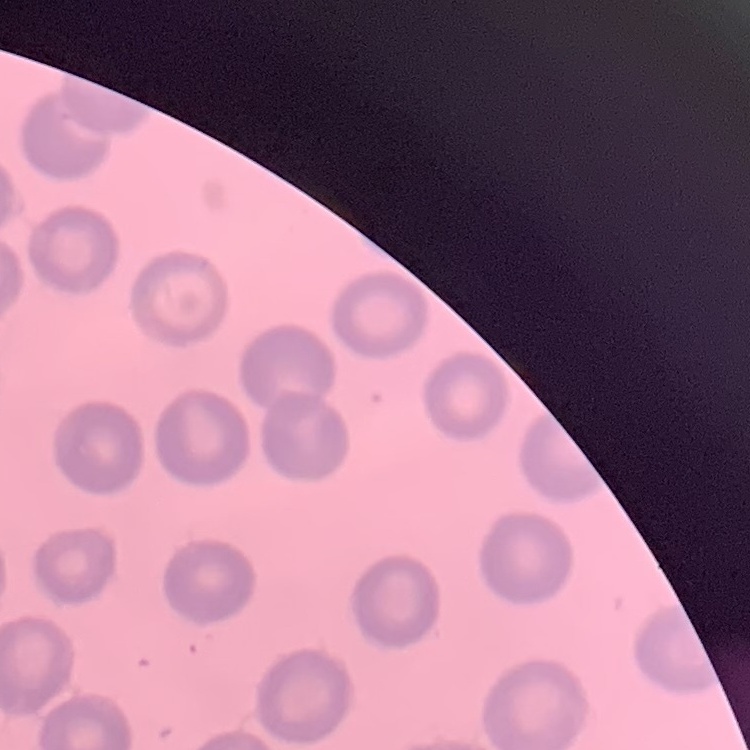
erythrocyte morphology = no rouleaux formation
image type = square crop of a larger photomicrograph
preparation = thin blood film
stain = Field's or Giemsa